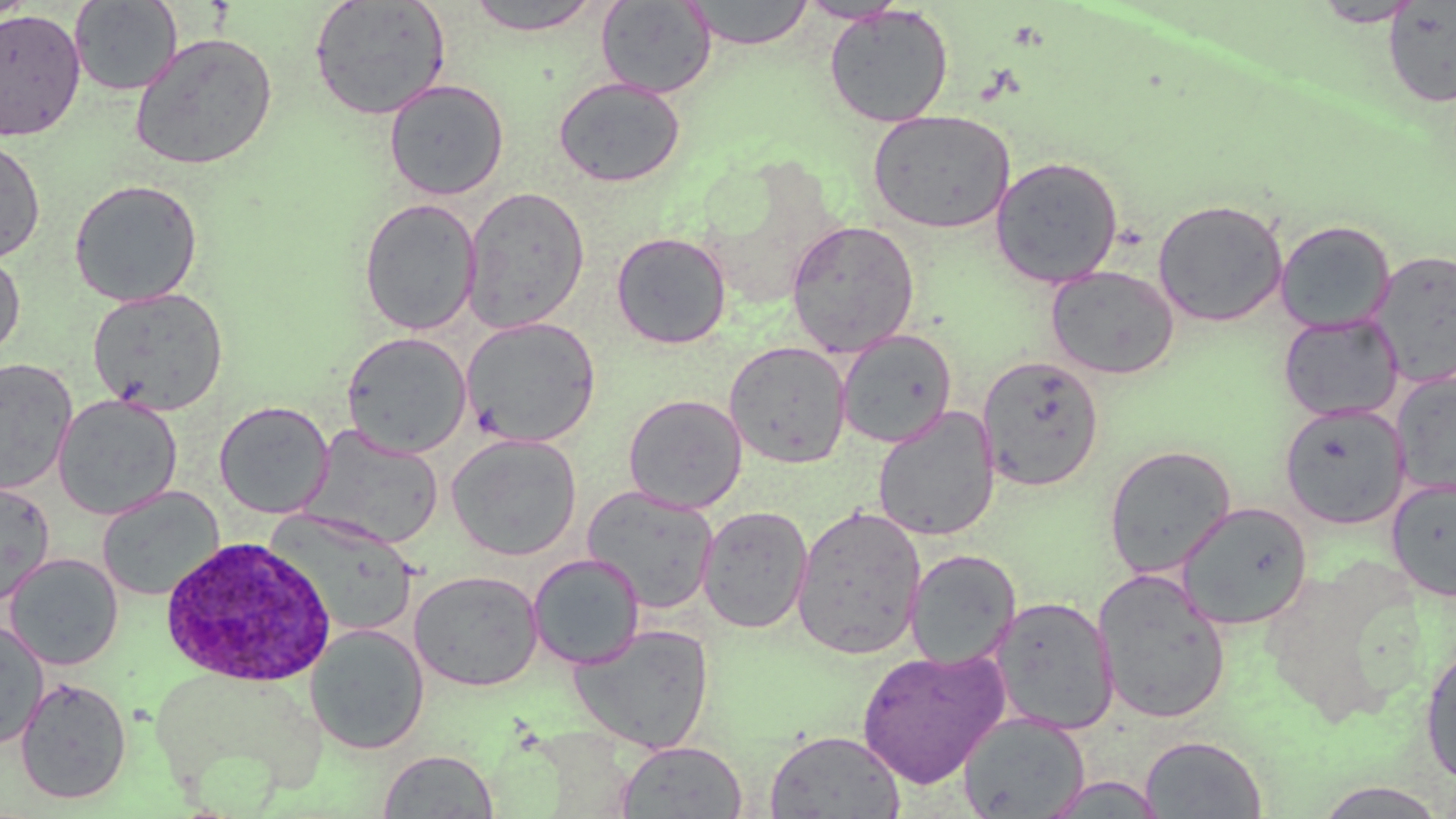

slide_level_diagnosis: Plasmodium ovale
field_of_view: single
uninfected_red_blood_cell_locations: 'approximate bounding boxes as [x1, y1, x2, y2] in pixels: [308, 0, 451, 121], [463, 0, 605, 35], [685, 0, 815, 49], [798, 0, 908, 23], [69, 1, 182, 96], [596, 1, 717, 98], [1312, 1, 1422, 27], [1383, 2, 1456, 109], [824, 5, 953, 128], [0, 8, 86, 143], [129, 31, 278, 171], [553, 76, 686, 188], [384, 78, 509, 200], [868, 109, 1015, 234], [0, 136, 45, 264], [990, 155, 1124, 288], [68, 178, 204, 307], [462, 186, 590, 333], [358, 197, 482, 335], [1153, 198, 1289, 326], [785, 219, 921, 357], [1275, 219, 1395, 332], [611, 231, 732, 349], [0, 249, 26, 360], [1370, 250, 1456, 385], [1045, 266, 1180, 379], [87, 287, 229, 415], [1279, 313, 1402, 421], [461, 316, 602, 447], [836, 329, 957, 448], [341, 332, 472, 457], [724, 341, 851, 468], [978, 355, 1105, 491], [0, 357, 78, 494], [1393, 370, 1456, 499], [624, 393, 747, 513], [53, 394, 182, 519], [214, 400, 334, 519], [1279, 403, 1410, 528], [872, 407, 1000, 542], [302, 425, 444, 549], [446, 433, 583, 560], [1104, 444, 1237, 578], [1386, 477, 1456, 602], [0, 480, 56, 606], [581, 485, 720, 612], [96, 486, 224, 601], [1177, 501, 1313, 629], [791, 504, 927, 660], [697, 505, 814, 635], [268, 511, 420, 638], [904, 549, 1021, 669], [4, 553, 124, 670], [528, 553, 645, 670], [409, 569, 544, 691], [1092, 569, 1231, 725], [990, 595, 1119, 735], [0, 618, 49, 749], [568, 622, 715, 753], [304, 624, 430, 755], [1420, 644, 1456, 786], [855, 646, 1009, 788], [146, 662, 327, 806], [14, 676, 132, 804], [959, 711, 1090, 818], [765, 729, 905, 817], [1140, 735, 1268, 818], [616, 741, 748, 818], [378, 749, 498, 818], [1037, 774, 1166, 818]'
plasmodium_ovale_infected_red_blood_cell_locations: 'approximate bounding boxes as [x1, y1, x2, y2] in pixels: [154, 537, 331, 689]'
stain: May-Grünwald-Giemsa
modality: light microscopy
magnification: 1000x
preparation: thin blood smear
image_size: 1456×819 pixels